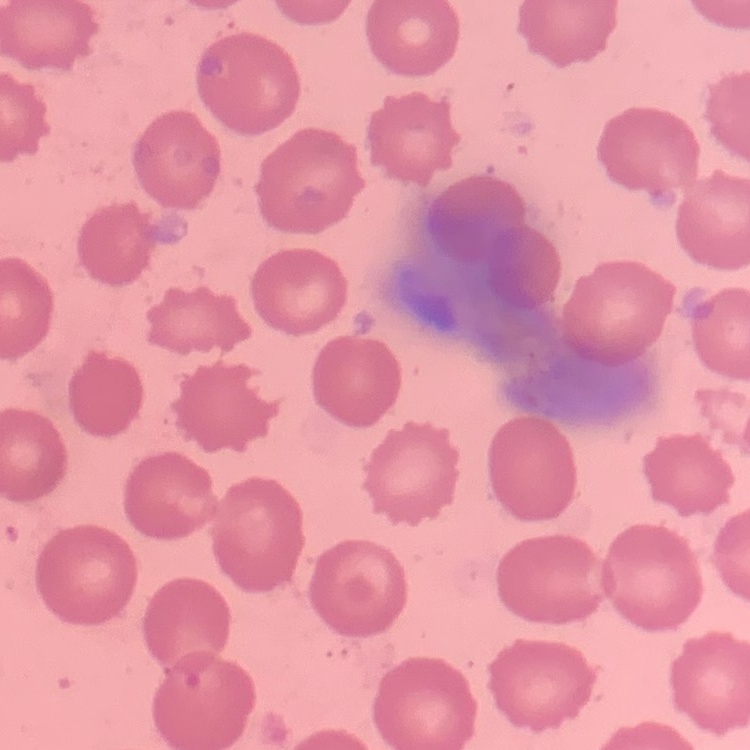

Summary:
  - Erythrocyte morphology: no rouleaux formation
  - Image type: square crop of a larger photomicrograph
  - Preparation: thin blood film
  - Stain: Field's or Giemsa